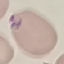

Result: malaria parasites identified. Photographed with a smartphone camera at the microscope eyepiece. Automatically extracted cell patch, resized to 64 × 64 pixels. Thin blood smear. Giemsa stain.